Assess this cell for malaria.
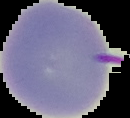

It is uninfected.

Summary:
  - Preparation: thin blood film
  - Image size: 130×118 pixels
  - Image type: segmented cell region with the area outside set to black